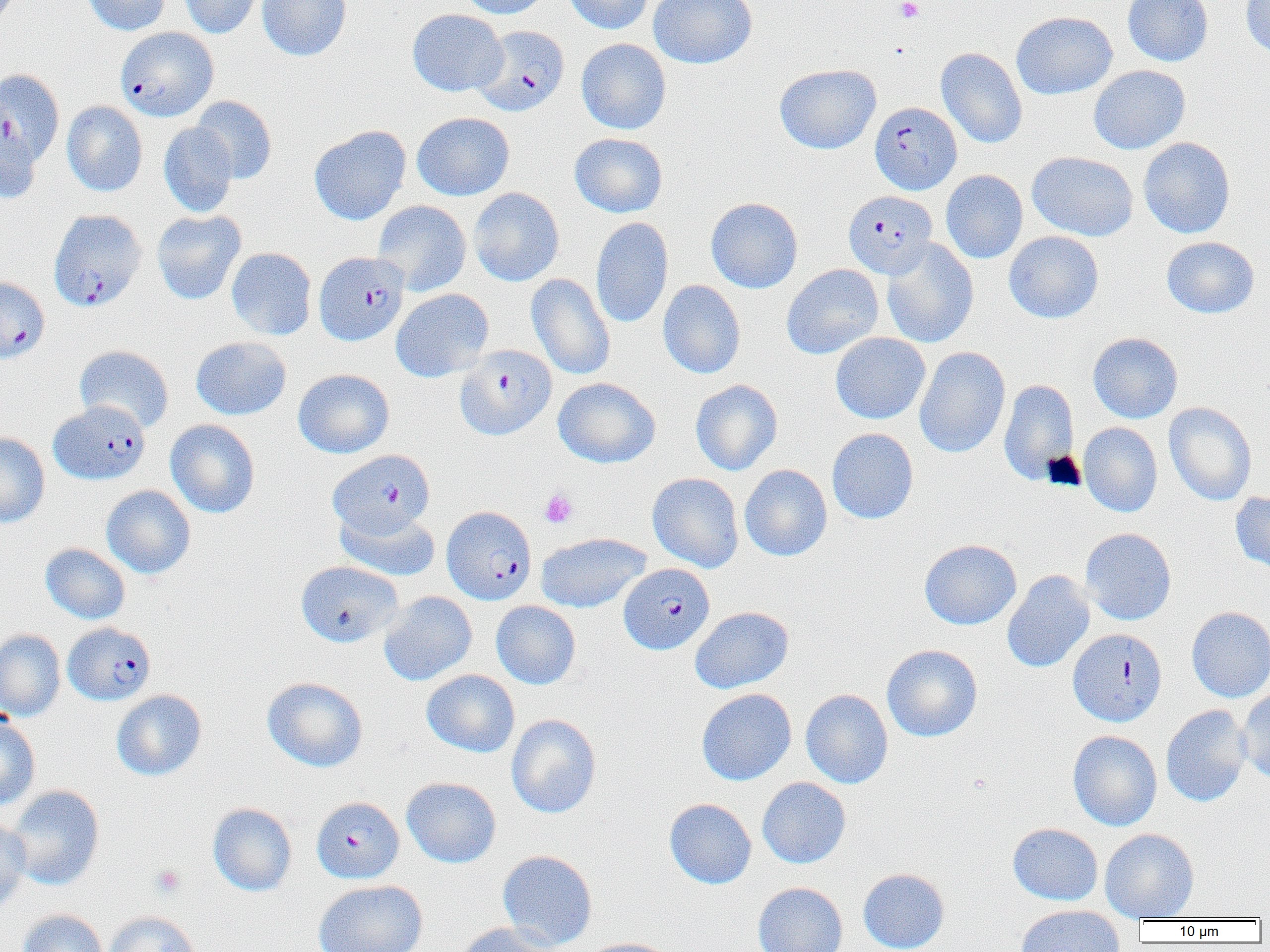
Approximate bounding boxes as named x1/y1/x2/y2 corners in pixels. Plasmodium falciparum-infected red blood cell locations (subset): (x1=475, y1=25, x2=569, y2=116), (x1=0, y1=68, x2=65, y2=169), (x1=870, y1=101, x2=962, y2=194), (x1=844, y1=190, x2=937, y2=278), (x1=48, y1=210, x2=146, y2=312), (x1=314, y1=251, x2=409, y2=346), (x1=0, y1=276, x2=49, y2=363), (x1=455, y1=344, x2=556, y2=440), (x1=49, y1=400, x2=150, y2=484), (x1=328, y1=449, x2=435, y2=538), (x1=440, y1=505, x2=535, y2=604), (x1=619, y1=563, x2=714, y2=654), (x1=63, y1=622, x2=155, y2=706), (x1=1067, y1=628, x2=1167, y2=726), (x1=319, y1=797, x2=412, y2=885). Uninfected red blood cell locations (subset): (x1=82, y1=0, x2=170, y2=35), (x1=181, y1=0, x2=265, y2=38), (x1=257, y1=0, x2=351, y2=61), (x1=454, y1=0, x2=551, y2=19), (x1=563, y1=0, x2=655, y2=34), (x1=648, y1=0, x2=757, y2=69), (x1=1122, y1=0, x2=1213, y2=66), (x1=1241, y1=0, x2=1270, y2=59), (x1=407, y1=9, x2=508, y2=96), (x1=1011, y1=11, x2=1117, y2=100), (x1=576, y1=38, x2=671, y2=134), (x1=936, y1=47, x2=1027, y2=149), (x1=774, y1=63, x2=881, y2=154), (x1=1089, y1=65, x2=1190, y2=154), (x1=190, y1=96, x2=277, y2=184), (x1=62, y1=101, x2=147, y2=196), (x1=412, y1=112, x2=515, y2=200), (x1=0, y1=114, x2=40, y2=204), (x1=158, y1=122, x2=239, y2=217), (x1=309, y1=125, x2=411, y2=225), (x1=569, y1=133, x2=668, y2=218), (x1=1138, y1=137, x2=1236, y2=238), (x1=1027, y1=151, x2=1138, y2=241), (x1=941, y1=170, x2=1028, y2=263), (x1=469, y1=188, x2=564, y2=287), (x1=706, y1=197, x2=803, y2=293), (x1=372, y1=200, x2=471, y2=296), (x1=151, y1=210, x2=246, y2=305), (x1=591, y1=217, x2=674, y2=329), (x1=1004, y1=231, x2=1104, y2=323), (x1=1161, y1=236, x2=1259, y2=318), (x1=881, y1=238, x2=979, y2=348), (x1=226, y1=247, x2=317, y2=340), (x1=781, y1=264, x2=884, y2=359), (x1=526, y1=273, x2=615, y2=380), (x1=658, y1=280, x2=746, y2=379), (x1=391, y1=289, x2=493, y2=382), (x1=831, y1=332, x2=930, y2=424), (x1=1088, y1=332, x2=1183, y2=423), (x1=191, y1=336, x2=291, y2=420), (x1=73, y1=344, x2=174, y2=432), (x1=914, y1=347, x2=1010, y2=458), (x1=293, y1=369, x2=394, y2=458), (x1=553, y1=377, x2=661, y2=468), (x1=999, y1=379, x2=1078, y2=485), (x1=690, y1=380, x2=782, y2=476), (x1=1164, y1=402, x2=1257, y2=505), (x1=1078, y1=418, x2=1255, y2=509), (x1=165, y1=419, x2=260, y2=518), (x1=1079, y1=422, x2=1162, y2=517), (x1=826, y1=428, x2=919, y2=525), (x1=0, y1=432, x2=50, y2=528), (x1=739, y1=464, x2=832, y2=561), (x1=647, y1=473, x2=744, y2=572), (x1=101, y1=485, x2=196, y2=579), (x1=1230, y1=490, x2=1270, y2=576), (x1=335, y1=506, x2=441, y2=580), (x1=1080, y1=528, x2=1176, y2=625), (x1=536, y1=532, x2=650, y2=613), (x1=919, y1=539, x2=1022, y2=630), (x1=40, y1=543, x2=130, y2=624), (x1=295, y1=561, x2=404, y2=647), (x1=1002, y1=570, x2=1095, y2=673), (x1=379, y1=591, x2=477, y2=686), (x1=491, y1=600, x2=581, y2=689), (x1=689, y1=606, x2=793, y2=693), (x1=1186, y1=606, x2=1270, y2=702), (x1=0, y1=629, x2=65, y2=721), (x1=882, y1=644, x2=983, y2=742), (x1=421, y1=669, x2=519, y2=757), (x1=262, y1=676, x2=368, y2=772), (x1=696, y1=688, x2=797, y2=785), (x1=111, y1=689, x2=207, y2=781), (x1=801, y1=689, x2=893, y2=789), (x1=1237, y1=689, x2=1270, y2=784), (x1=1160, y1=705, x2=1252, y2=806), (x1=0, y1=714, x2=41, y2=812), (x1=506, y1=714, x2=601, y2=818), (x1=1067, y1=730, x2=1162, y2=830), (x1=401, y1=777, x2=501, y2=868), (x1=757, y1=777, x2=851, y2=868), (x1=6, y1=785, x2=105, y2=890), (x1=664, y1=798, x2=756, y2=889), (x1=208, y1=802, x2=297, y2=896), (x1=0, y1=816, x2=31, y2=914), (x1=1007, y1=823, x2=1103, y2=906), (x1=1100, y1=828, x2=1199, y2=921), (x1=497, y1=849, x2=597, y2=951), (x1=858, y1=868, x2=949, y2=952), (x1=313, y1=880, x2=427, y2=952), (x1=753, y1=881, x2=848, y2=952), (x1=1014, y1=904, x2=1125, y2=952), (x1=17, y1=909, x2=108, y2=952), (x1=102, y1=911, x2=201, y2=952), (x1=454, y1=923, x2=558, y2=952), (x1=582, y1=937, x2=682, y2=952). Platelet locations: (x1=895, y1=0, x2=923, y2=23), (x1=539, y1=489, x2=578, y2=528), (x1=151, y1=865, x2=184, y2=897). Slide-level diagnosis: Plasmodium falciparum. Image is 1270×952 pixels. Single field of view. Thin blood smear. Light microscopy. Captured at 1000x magnification.